Give the position of every malaria parasite.
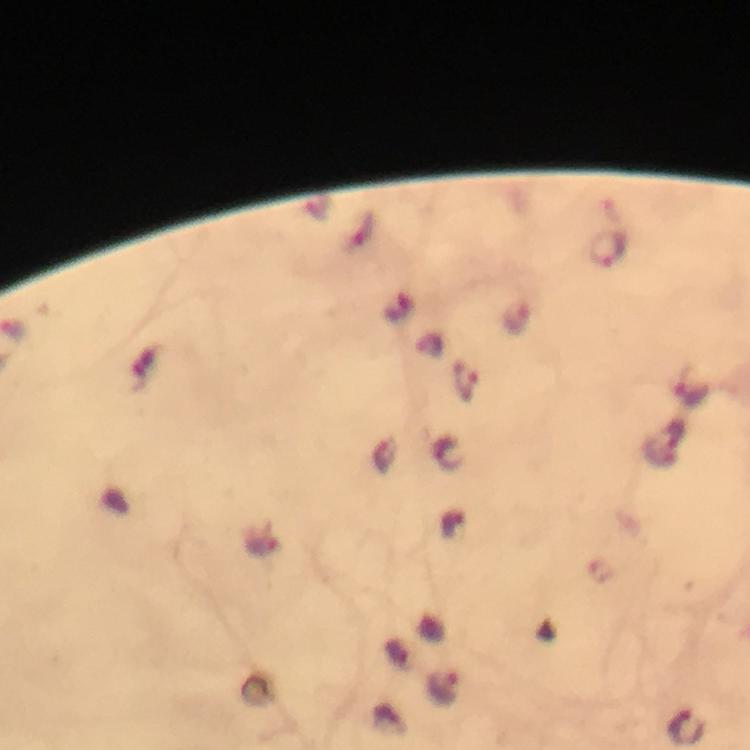
Approximate centers as (x, y) in pixels.
Malaria parasites: (610, 249), (517, 316), (467, 380), (444, 688), (688, 727).

Summary:
  - Context: from a diagnostic examination for malaria
  - Image size: 750×750 pixels
  - Cropped from: one field of view
  - Capture: smartphone photograph through a microscope
  - Preparation: thick smear
  - Immersion oil: applied
  - Stain: Giemsa
  - Magnification: 100x